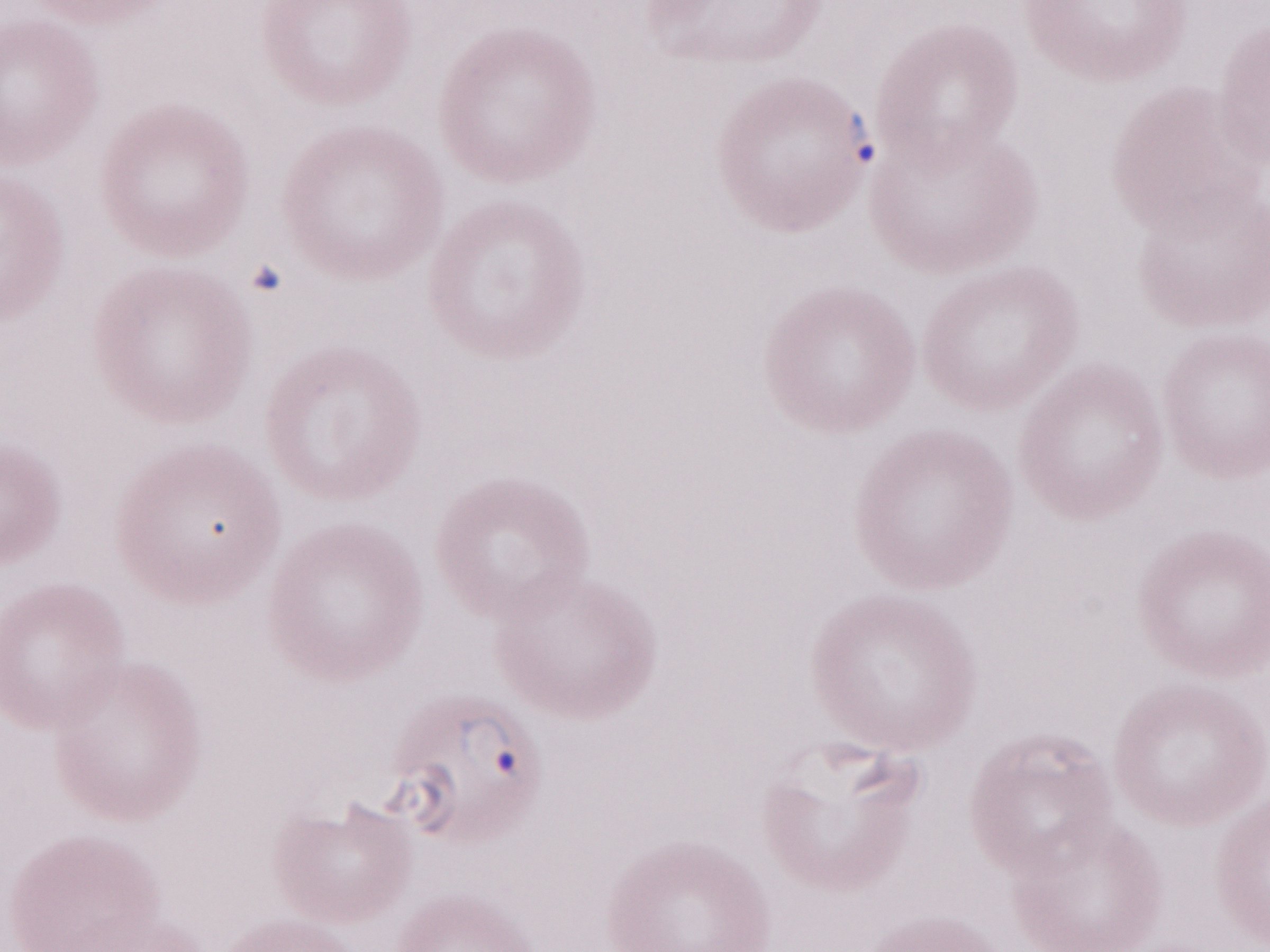 Thin blood film. Olympus BX43 microscope and DP73 digital camera. 1,000x magnification. May-Grünwald-Giemsa stain. Single field of view. Patient-level malaria diagnosis: positive. Image is 1270×952 pixels.